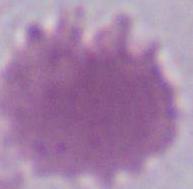 Micrograph. An erythrocyte is seen. 1000x magnification.